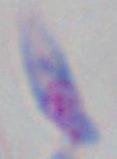

Summary:
  - Modality: photomicrograph
  - Identification: Toxoplasma gondii
  - Magnification: 1000x